Assess this cell for malaria.
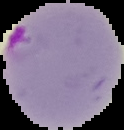

Parasitized.

image type = segmented cell region with the area outside set to black
preparation = thin blood smear
image size = 124×130 pixels